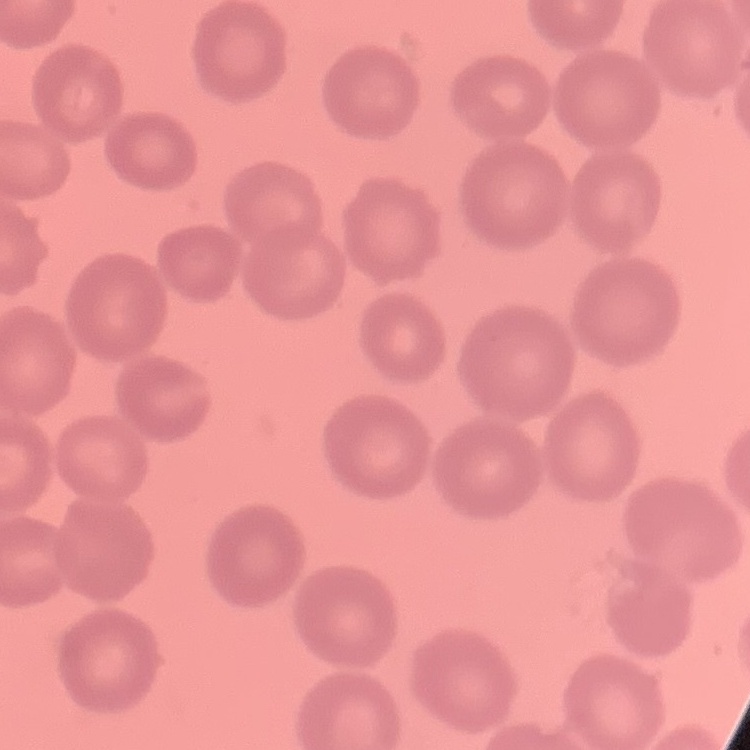
The red blood cells exhibit no rouleaux formation. Field's or Giemsa stain. Square crop of a larger photomicrograph. Thin peripheral smear.